Assess this cell for malaria.
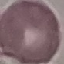

Uninfected.

image_type: cell patch, automatically extracted from a larger field of view and resized to 64 × 64 pixels
preparation: thin blood film
capture: smartphone through the microscope eyepiece
stain: Giemsa